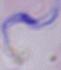

magnification: 1000x
modality: micrograph
identification: trypanosome